Locate every malaria parasite by life-cycle stage, and every leukocyte.
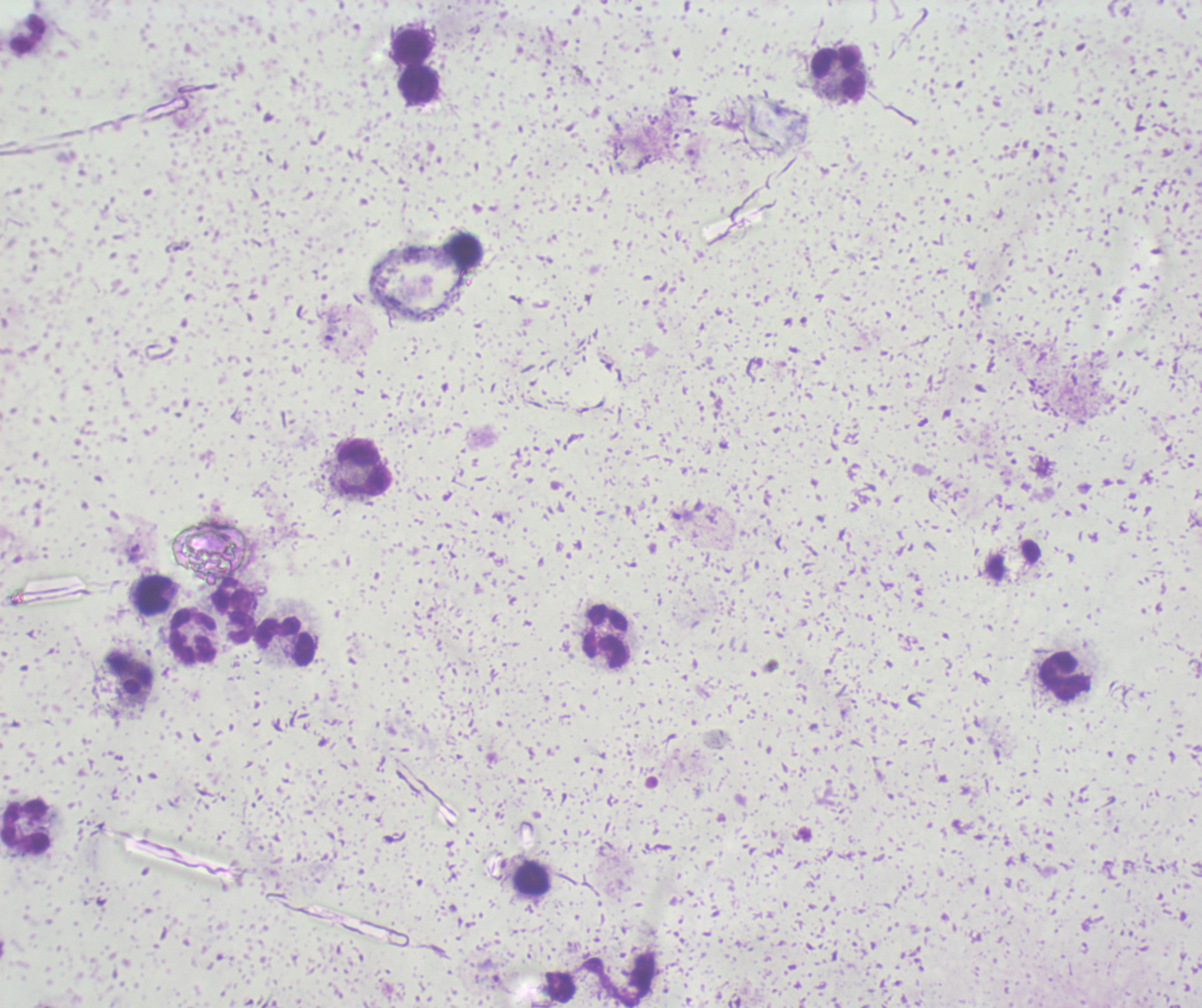
Approximate centers as [x, y] in pixels.
Trophozoites: [332, 333], [135, 549].
Gametocytes: [130, 680].
No schizont forms observed.
Leukocytes: [27, 33], [411, 46], [839, 73], [418, 85], [363, 469], [1013, 560], [152, 593], [233, 611], [194, 637], [606, 637], [287, 641], [1065, 676], [25, 827], [530, 879].

Summary:
  - Image size: 1202×1008 pixels
  - Stain: Romanowsky
  - Background quality: unsatisfactory
  - Context: previously used in a real diagnosis
  - Field of view: single
  - Magnification: 100x
  - Preparation: thick smear of blood